State which parasite is depicted.
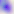

This is Toxoplasma gondii.

Summary:
  - Modality: photomicrograph
  - Magnification: 400x